State which parasite is depicted.
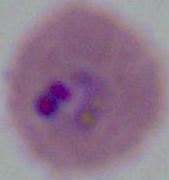

Plasmodium.

magnification: 400x or 1000x
modality: micrograph